Name the blood parasite species.
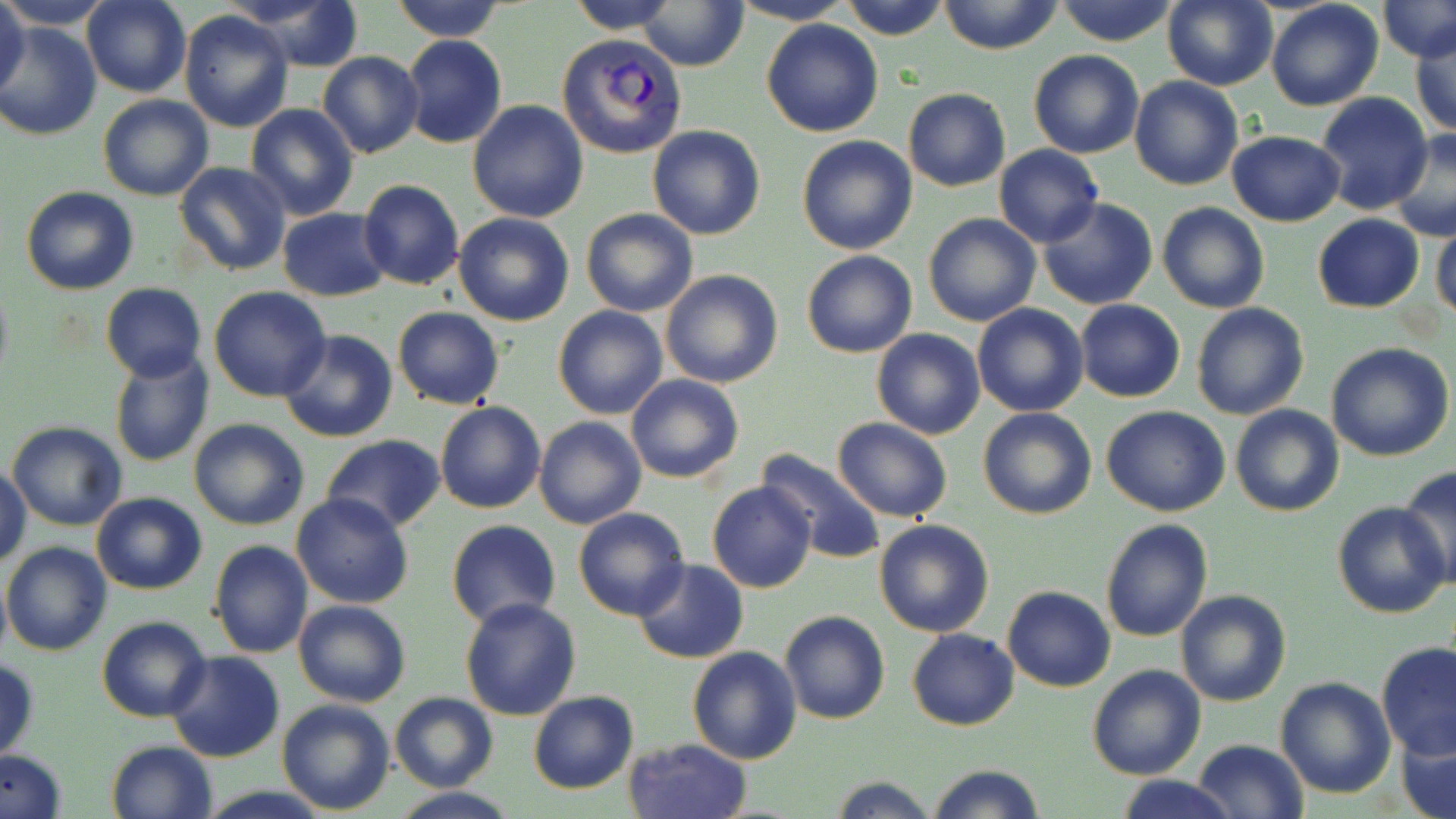

Plasmodium vivax.

Approximate bounding boxes as named x1/y1/x2/y2 corners in pixels. Plasmodium vivax-infected red blood cell locations: (x1=557, y1=34, x2=687, y2=157). Uninfected red blood cell locations: (x1=0, y1=0, x2=115, y2=30), (x1=0, y1=0, x2=30, y2=106), (x1=82, y1=0, x2=192, y2=99), (x1=227, y1=0, x2=365, y2=72), (x1=390, y1=0, x2=507, y2=42), (x1=566, y1=0, x2=680, y2=33), (x1=727, y1=0, x2=856, y2=26), (x1=838, y1=0, x2=952, y2=41), (x1=937, y1=0, x2=1066, y2=55), (x1=1052, y1=0, x2=1182, y2=46), (x1=1161, y1=0, x2=1278, y2=90), (x1=1265, y1=0, x2=1384, y2=111), (x1=1380, y1=0, x2=1456, y2=61), (x1=636, y1=2, x2=751, y2=70), (x1=179, y1=10, x2=296, y2=131), (x1=761, y1=18, x2=884, y2=138), (x1=1, y1=20, x2=102, y2=142), (x1=1409, y1=24, x2=1455, y2=138), (x1=399, y1=35, x2=508, y2=148), (x1=1029, y1=50, x2=1145, y2=158), (x1=317, y1=52, x2=424, y2=159), (x1=1129, y1=76, x2=1244, y2=191), (x1=902, y1=89, x2=1011, y2=191), (x1=1315, y1=93, x2=1432, y2=215), (x1=98, y1=94, x2=213, y2=200), (x1=467, y1=100, x2=591, y2=222), (x1=245, y1=103, x2=359, y2=220), (x1=648, y1=125, x2=765, y2=240), (x1=1387, y1=128, x2=1456, y2=241), (x1=1228, y1=130, x2=1345, y2=226), (x1=796, y1=135, x2=918, y2=254), (x1=993, y1=144, x2=1104, y2=248), (x1=173, y1=161, x2=290, y2=277), (x1=357, y1=178, x2=465, y2=290), (x1=21, y1=185, x2=139, y2=295), (x1=1038, y1=198, x2=1159, y2=311), (x1=1157, y1=202, x2=1269, y2=313), (x1=276, y1=208, x2=393, y2=302), (x1=580, y1=209, x2=698, y2=317), (x1=1431, y1=210, x2=1456, y2=324), (x1=454, y1=212, x2=574, y2=326), (x1=923, y1=213, x2=1042, y2=328), (x1=1312, y1=213, x2=1426, y2=313), (x1=800, y1=250, x2=918, y2=358), (x1=659, y1=269, x2=784, y2=388), (x1=0, y1=278, x2=13, y2=390), (x1=100, y1=283, x2=207, y2=382), (x1=208, y1=286, x2=331, y2=402), (x1=1074, y1=298, x2=1185, y2=403), (x1=1191, y1=303, x2=1308, y2=420), (x1=972, y1=304, x2=1088, y2=416), (x1=553, y1=305, x2=667, y2=419), (x1=392, y1=308, x2=505, y2=409), (x1=278, y1=329, x2=398, y2=442), (x1=871, y1=329, x2=986, y2=439), (x1=1325, y1=342, x2=1453, y2=461), (x1=109, y1=350, x2=215, y2=469), (x1=626, y1=374, x2=744, y2=484), (x1=434, y1=402, x2=546, y2=514), (x1=1230, y1=404, x2=1343, y2=516), (x1=1100, y1=405, x2=1231, y2=516), (x1=978, y1=406, x2=1097, y2=521), (x1=533, y1=415, x2=645, y2=530), (x1=188, y1=417, x2=309, y2=530), (x1=832, y1=418, x2=955, y2=523), (x1=7, y1=422, x2=127, y2=531), (x1=320, y1=433, x2=447, y2=532), (x1=755, y1=448, x2=886, y2=566), (x1=1, y1=461, x2=30, y2=571), (x1=1397, y1=465, x2=1456, y2=586), (x1=707, y1=481, x2=817, y2=594), (x1=92, y1=493, x2=206, y2=594), (x1=292, y1=493, x2=414, y2=608), (x1=1333, y1=501, x2=1452, y2=619), (x1=572, y1=507, x2=689, y2=621), (x1=1100, y1=518, x2=1213, y2=642), (x1=874, y1=519, x2=995, y2=637), (x1=445, y1=520, x2=562, y2=629), (x1=209, y1=539, x2=314, y2=658), (x1=2, y1=541, x2=114, y2=656), (x1=632, y1=558, x2=748, y2=663), (x1=1002, y1=585, x2=1115, y2=692), (x1=1174, y1=590, x2=1291, y2=707), (x1=459, y1=597, x2=582, y2=720), (x1=293, y1=599, x2=410, y2=708), (x1=779, y1=610, x2=889, y2=725), (x1=97, y1=616, x2=212, y2=722), (x1=907, y1=628, x2=1019, y2=731), (x1=1377, y1=644, x2=1456, y2=758), (x1=686, y1=645, x2=804, y2=764), (x1=166, y1=650, x2=285, y2=763), (x1=0, y1=659, x2=39, y2=761), (x1=1087, y1=664, x2=1208, y2=781), (x1=1274, y1=675, x2=1395, y2=800), (x1=528, y1=690, x2=638, y2=794), (x1=390, y1=693, x2=498, y2=793), (x1=277, y1=698, x2=395, y2=815), (x1=1396, y1=724, x2=1455, y2=819), (x1=623, y1=738, x2=752, y2=819), (x1=106, y1=739, x2=217, y2=818), (x1=1192, y1=739, x2=1310, y2=819), (x1=0, y1=749, x2=66, y2=819), (x1=927, y1=762, x2=1047, y2=819), (x1=1118, y1=774, x2=1235, y2=819), (x1=827, y1=775, x2=940, y2=818), (x1=196, y1=787, x2=337, y2=818), (x1=390, y1=787, x2=519, y2=818). Optical microscopy. 1000x magnification. Image is 1456×819 pixels. Thin blood film. One field of a larger specimen. May-Grünwald-Giemsa stain.